Identify the parasite.
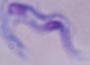

This is a trypanosome.

Captured at 1000x magnification. Micrograph.